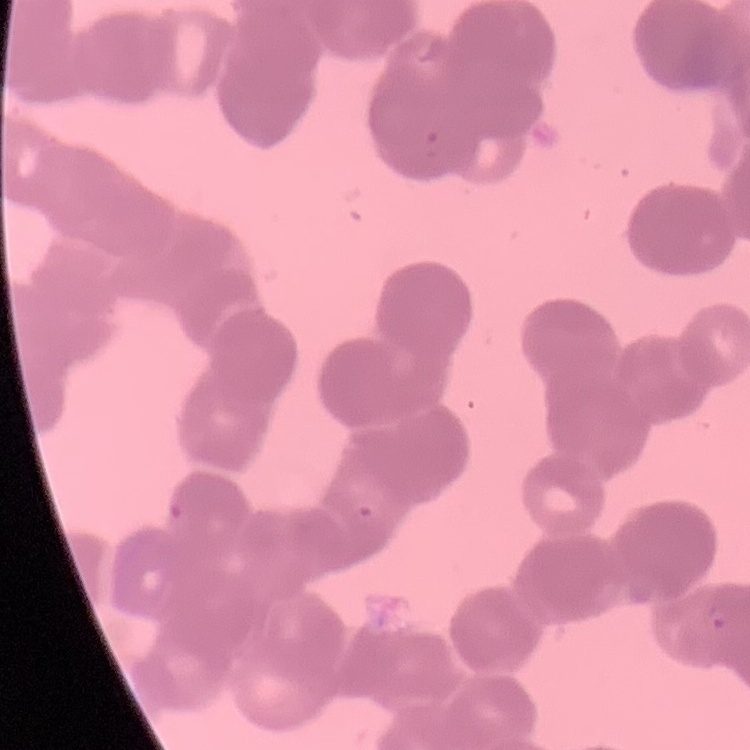
Summary:
  - Red blood cell morphology: rouleaux formation
  - Preparation: thin blood smear
  - Image type: one tile cut from a larger photomicrograph
  - Stain: Field's or Giemsa